Classify this cell by malaria status.
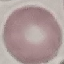

Uninfected.

Giemsa-stained preparation. Acquired by smartphone through the microscope eyepiece. Thin blood film. Cell patch, automatically extracted from a larger field of view and resized to 64 × 64 pixels.